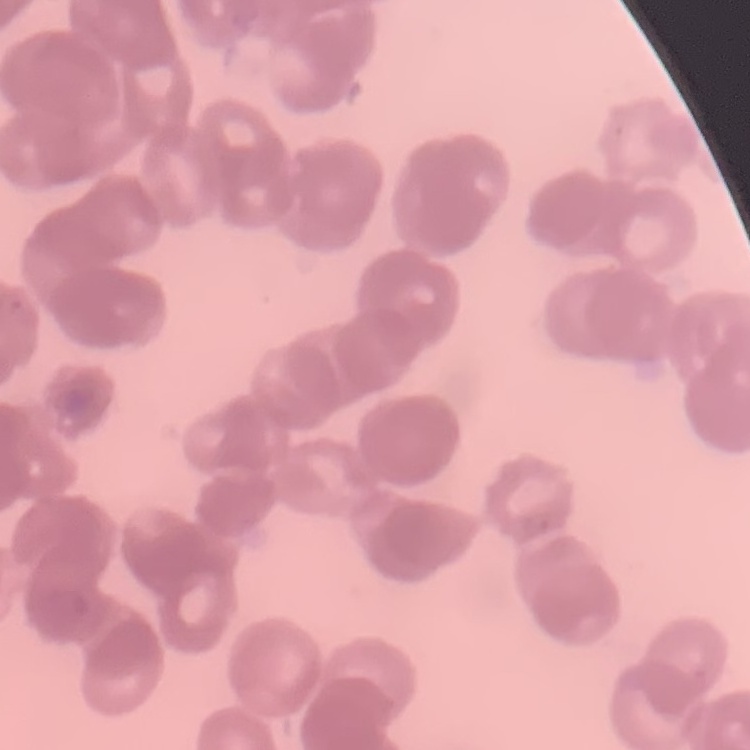
erythrocyte morphology = rouleaux formation
image type = one tile cut from a larger photomicrograph
preparation = thin blood smear
stain = Field's or Giemsa